Report the malaria status of this cell.
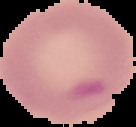

It is uninfected.

Summary:
  - Image type: cell region segmented out of the field of view; surrounding area masked to black
  - Preparation: thin blood smear
  - Image size: 136×127 pixels